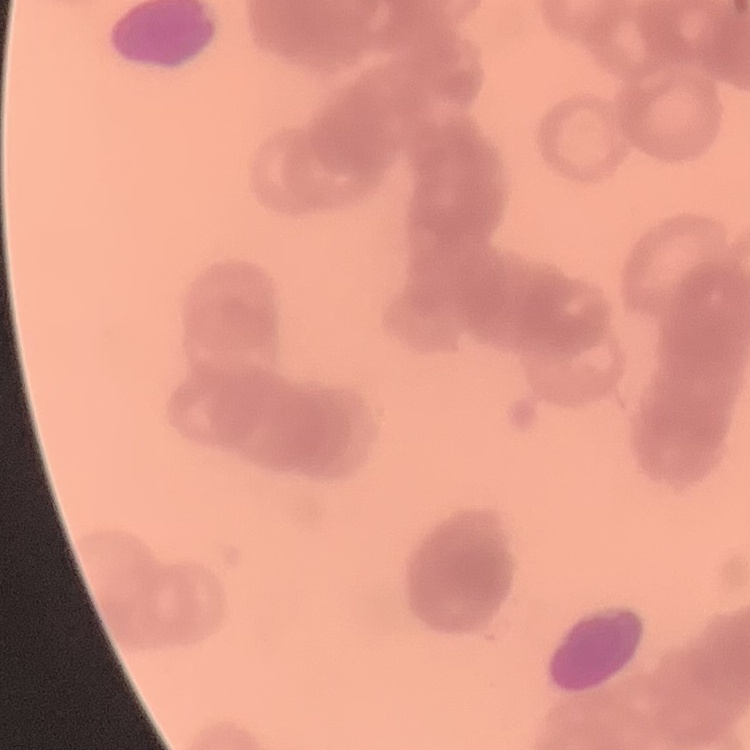
The red blood cells show rouleaux formation. One tile cut from a larger photomicrograph. Thin peripheral smear. Stained with either Field's or Giemsa.